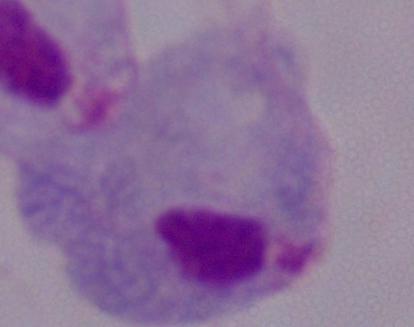
Summary:
  - Identification: trichomonad
  - Modality: micrograph
  - Magnification: 1000x